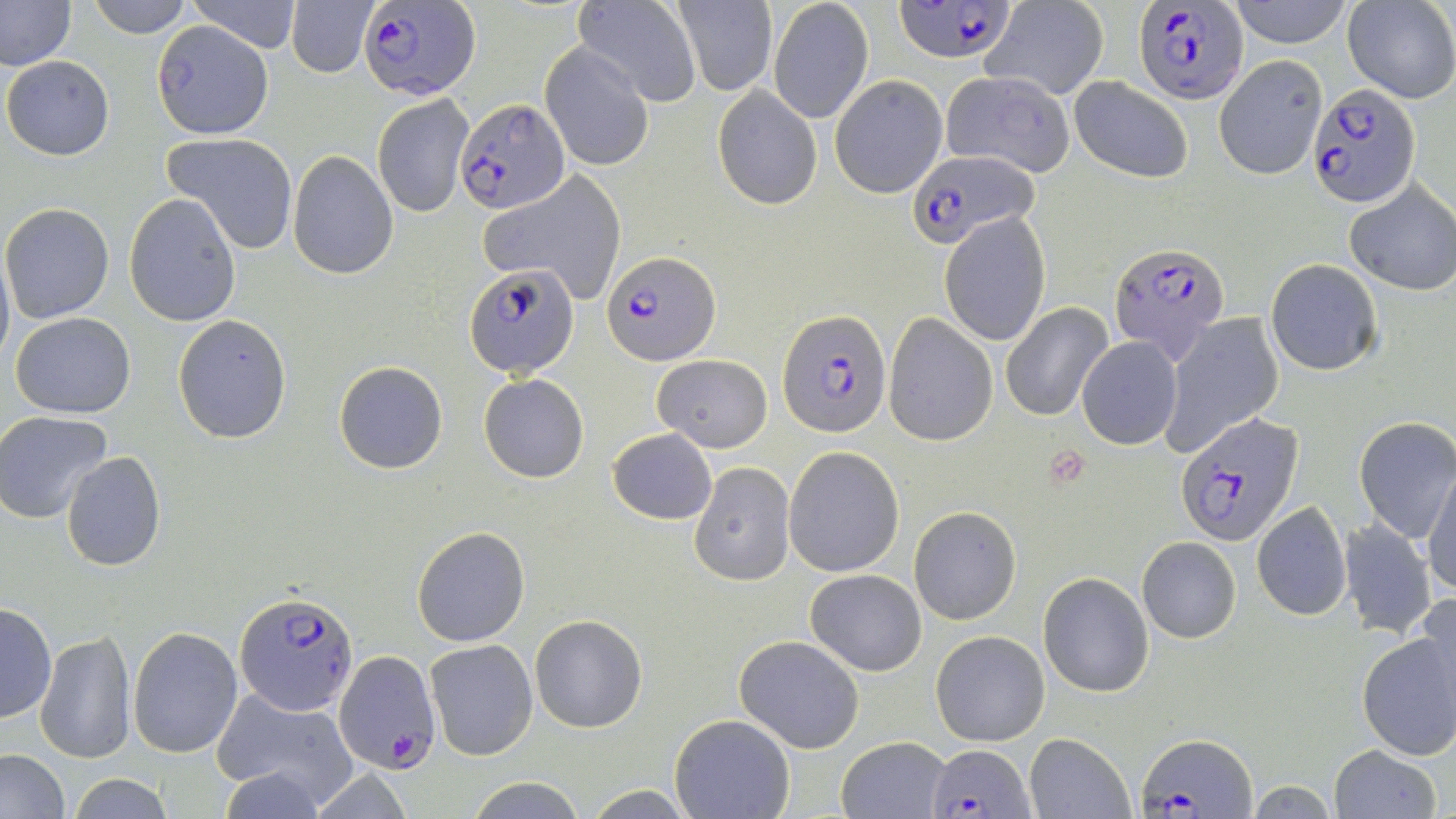
Summary:
  - Coordinate format: approximate bounding boxes as (x1, y1, x2, y2) in pixels
  - Plasmodium falciparum-infected red blood cell locations: (897, 0, 1019, 63), (361, 1, 481, 100), (1137, 2, 1247, 102), (1307, 84, 1419, 208), (455, 99, 569, 214), (909, 152, 1034, 248), (1111, 242, 1231, 363), (603, 252, 720, 366), (464, 261, 580, 379), (780, 309, 891, 438), (1173, 412, 1302, 548), (235, 589, 357, 713), (335, 651, 440, 772), (1136, 734, 1257, 816), (926, 742, 1037, 818)
  - Uninfected red blood cell locations: (0, 0, 77, 70), (86, 0, 193, 35), (573, 0, 699, 107), (981, 0, 1109, 100), (1230, 0, 1354, 48), (1342, 0, 1456, 102), (184, 1, 304, 52), (285, 1, 379, 78), (673, 1, 777, 95), (769, 3, 872, 123), (152, 19, 274, 138), (540, 44, 654, 172), (1213, 54, 1328, 179), (2, 55, 115, 160), (939, 70, 1075, 175), (830, 75, 947, 198), (1068, 75, 1193, 185), (713, 84, 822, 211), (372, 93, 474, 217), (161, 132, 299, 253), (286, 151, 398, 279), (477, 169, 627, 304), (1343, 180, 1456, 296), (123, 195, 243, 327), (1, 202, 114, 323), (939, 213, 1051, 346), (0, 245, 13, 373), (1265, 259, 1382, 377), (1001, 303, 1114, 422), (10, 313, 135, 419), (883, 313, 998, 447), (1160, 314, 1284, 455), (173, 315, 293, 444), (1077, 337, 1182, 450), (652, 354, 773, 453), (335, 362, 449, 474), (479, 373, 589, 483), (0, 409, 113, 523), (1355, 418, 1456, 541), (607, 428, 717, 525), (784, 446, 904, 576), (61, 451, 167, 572), (1423, 459, 1456, 599), (688, 462, 795, 586), (1251, 502, 1351, 622), (910, 506, 1020, 625), (1338, 519, 1438, 637), (410, 526, 529, 647), (1137, 538, 1241, 643), (805, 568, 926, 676), (1038, 572, 1154, 697), (1415, 592, 1456, 708), (0, 601, 57, 723), (529, 614, 647, 733), (129, 625, 243, 758), (1356, 627, 1456, 763), (35, 629, 136, 764), (931, 630, 1050, 746), (734, 635, 865, 754), (426, 639, 537, 760), (211, 689, 360, 809), (670, 714, 796, 819), (1024, 733, 1133, 818), (837, 735, 950, 818), (1329, 744, 1442, 818), (0, 749, 69, 818), (66, 773, 175, 819), (463, 776, 589, 818), (1245, 781, 1339, 817), (579, 786, 702, 818)
  - Slide-level diagnosis: Plasmodium falciparum
  - Image size: 1456×819 pixels
  - Preparation: thin blood smear
  - Modality: optical microscopy
  - Magnification: 1000x
  - Field of view: one of a larger specimen
  - Stain: May-Grünwald-Giemsa